Assess this cell for malaria.
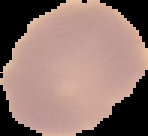

It is uninfected.

image type = cell region segmented out of the field of view; surrounding area masked to black
preparation = thin blood smear
image size = 148×136 pixels